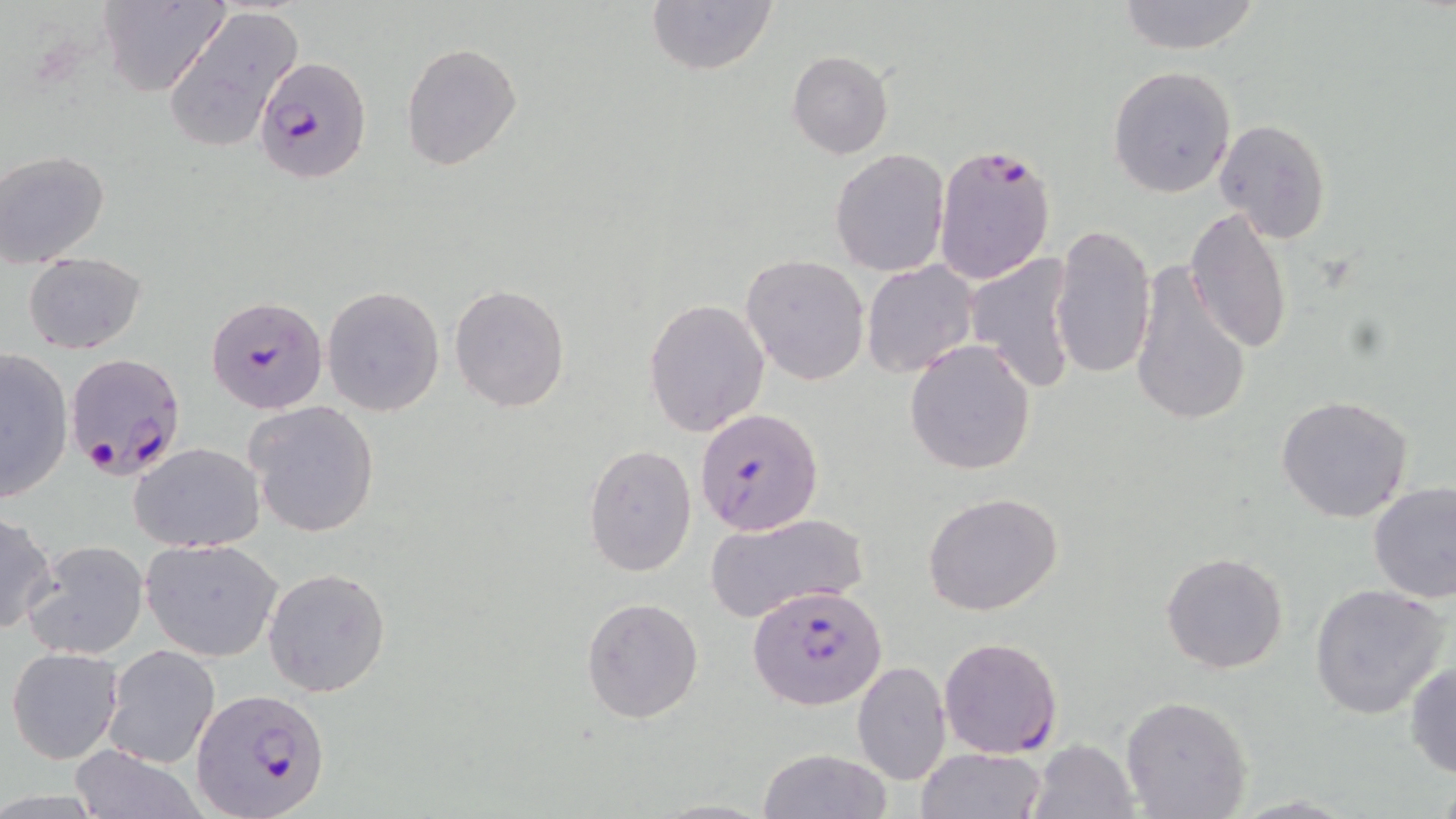
slide-level diagnosis = Plasmodium falciparum
magnification = 1000x
stain = May-Grünwald-Giemsa
image size = 1456×819 pixels
preparation = thin blood film
Plasmodium falciparum-infected red blood cell locations = approximate bounding boxes as (x1, y1, x2, y2) in pixels: (255, 56, 370, 184), (932, 140, 1057, 287), (206, 295, 328, 414), (63, 354, 187, 481), (694, 408, 823, 536), (748, 587, 886, 710), (938, 636, 1062, 757), (191, 686, 333, 819)
uninfected red blood cell locations = approximate bounding boxes as (x1, y1, x2, y2) in pixels: (99, 0, 225, 99), (649, 0, 778, 74), (1116, 0, 1262, 54), (160, 5, 304, 154), (400, 42, 522, 171), (787, 50, 892, 159), (1108, 65, 1237, 197), (1213, 118, 1331, 245), (829, 148, 950, 278), (0, 149, 111, 268), (1184, 207, 1293, 355), (1050, 222, 1155, 381), (965, 250, 1079, 393), (23, 251, 147, 354), (740, 254, 870, 387), (862, 260, 979, 379), (1128, 260, 1252, 431), (449, 283, 569, 412), (322, 284, 446, 417), (643, 298, 770, 437), (904, 339, 1037, 476), (0, 348, 73, 500), (1276, 394, 1414, 524), (246, 400, 381, 538), (130, 442, 265, 553), (583, 444, 698, 578), (1368, 481, 1456, 603), (922, 492, 1063, 617), (0, 512, 56, 636), (704, 513, 869, 623), (141, 538, 282, 661), (24, 540, 147, 659), (1160, 552, 1289, 674), (263, 566, 391, 698), (1308, 583, 1450, 718), (581, 595, 705, 724), (101, 644, 222, 768), (7, 646, 124, 764), (851, 661, 950, 785), (1405, 661, 1455, 779), (1120, 696, 1252, 819), (1028, 739, 1137, 819), (69, 744, 203, 819), (757, 748, 891, 819), (914, 748, 1049, 819)
field of view = one of a larger specimen
modality = optical microscopy